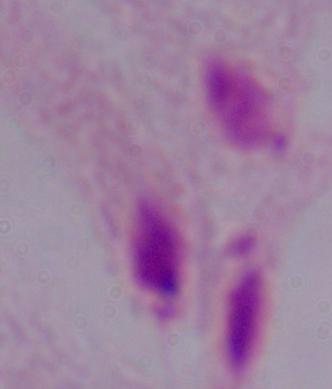

A trichomonad is shown. Photomicrograph. 1000x magnification.